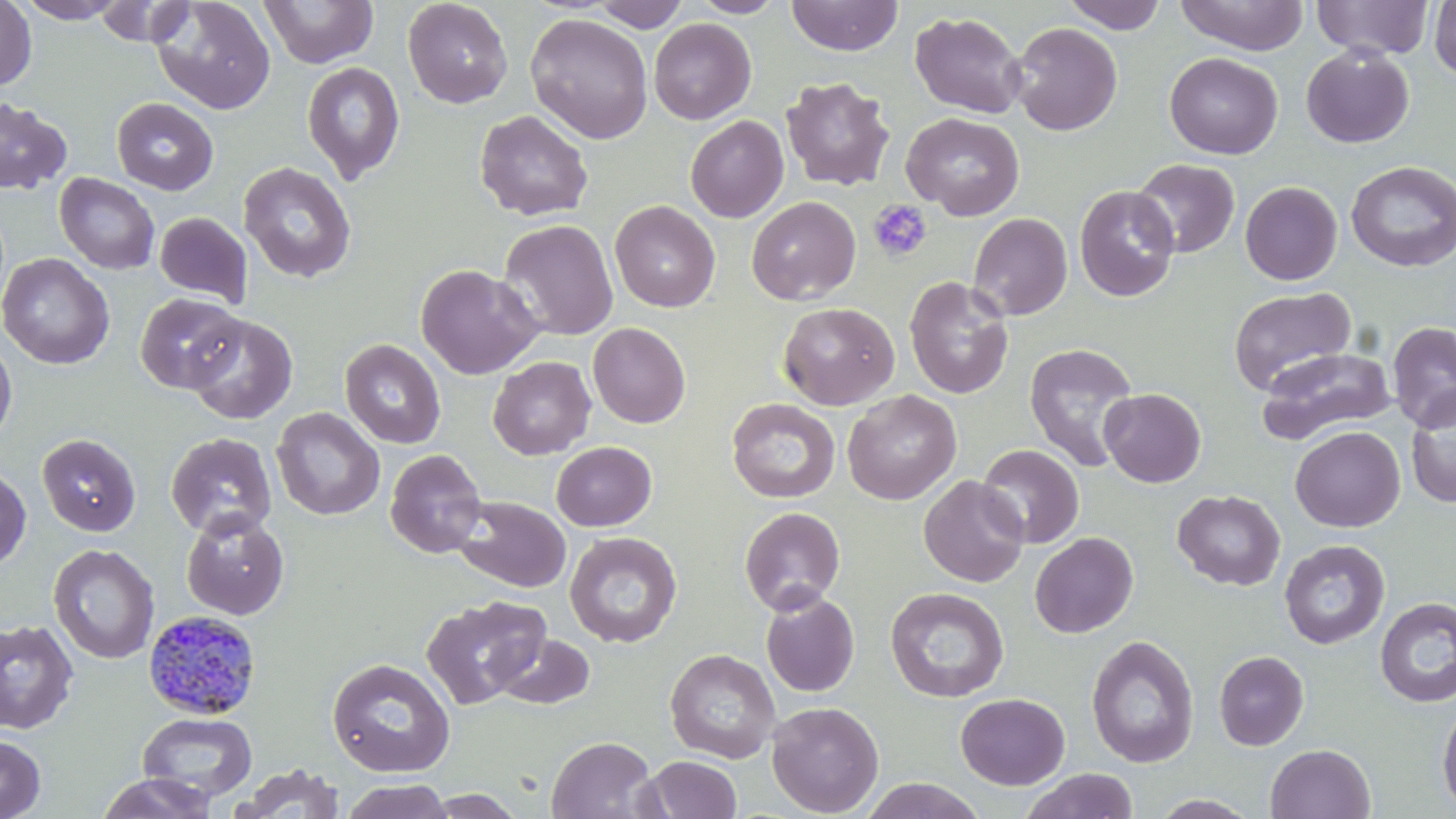
Approximate bounding boxes as (x1, y1, x2, y2) in pixels. Platelet locations: (868, 199, 933, 263). Plasmodium malariae-infected red blood cell locations: (142, 609, 261, 719). Uninfected red blood cell locations: (0, 0, 37, 92), (15, 0, 129, 24), (151, 0, 276, 115), (259, 0, 378, 69), (403, 0, 513, 109), (689, 0, 788, 18), (786, 0, 904, 56), (1061, 0, 1169, 33), (1175, 0, 1309, 55), (1313, 0, 1434, 60), (93, 1, 195, 47), (591, 1, 690, 31), (1428, 1, 1456, 84), (910, 11, 1027, 119), (525, 13, 653, 144), (649, 18, 756, 125), (1009, 22, 1123, 136), (1301, 45, 1414, 148), (1164, 52, 1283, 159), (301, 61, 404, 184), (780, 76, 895, 191), (0, 96, 73, 196), (111, 97, 218, 194), (474, 109, 594, 221), (901, 112, 1025, 220), (686, 115, 788, 223), (1130, 158, 1240, 257), (1345, 161, 1456, 272), (237, 162, 356, 284), (54, 173, 160, 275), (1240, 181, 1342, 285), (1074, 185, 1180, 302), (746, 196, 861, 305), (609, 200, 720, 312), (155, 212, 252, 306), (967, 213, 1072, 320), (499, 219, 619, 342), (0, 253, 115, 370), (415, 263, 543, 380), (904, 276, 1014, 399), (1229, 286, 1356, 396), (135, 293, 246, 394), (778, 301, 900, 410), (185, 314, 298, 425), (588, 322, 691, 428), (1387, 322, 1456, 431), (0, 333, 17, 446), (339, 339, 446, 448), (1024, 342, 1140, 472), (1256, 348, 1396, 444), (488, 356, 596, 459), (1405, 387, 1456, 508), (1099, 388, 1206, 487), (842, 390, 962, 505), (726, 398, 840, 503), (271, 408, 385, 520), (1290, 426, 1406, 532), (165, 432, 277, 539), (36, 433, 141, 536), (551, 441, 656, 531), (978, 444, 1085, 549), (385, 449, 488, 558), (0, 465, 31, 572), (918, 475, 1029, 587), (1172, 489, 1286, 591), (453, 496, 571, 593), (739, 506, 846, 615), (181, 511, 289, 619), (565, 532, 683, 647), (1030, 532, 1138, 638), (1279, 539, 1390, 649), (48, 544, 160, 664), (884, 586, 1009, 703), (760, 590, 860, 697), (420, 595, 549, 710), (1375, 597, 1456, 707), (0, 619, 79, 733), (492, 632, 596, 710), (1085, 635, 1200, 768), (665, 648, 781, 763), (1214, 651, 1309, 750), (327, 657, 455, 778), (955, 693, 1070, 789), (1437, 698, 1456, 816), (767, 701, 884, 817), (137, 712, 257, 802), (0, 734, 46, 819), (546, 735, 660, 819), (1265, 744, 1376, 819), (641, 756, 742, 818), (234, 764, 345, 818), (1020, 769, 1139, 819), (96, 772, 219, 818), (859, 777, 987, 819), (340, 779, 455, 819), (420, 790, 528, 818), (1148, 793, 1263, 818). Slide-level diagnosis: Plasmodium malariae. Single field of view. Thin blood smear. May-Grünwald-Giemsa stain. Light microscopy. Image is 1456×819 pixels. 1000x magnification.